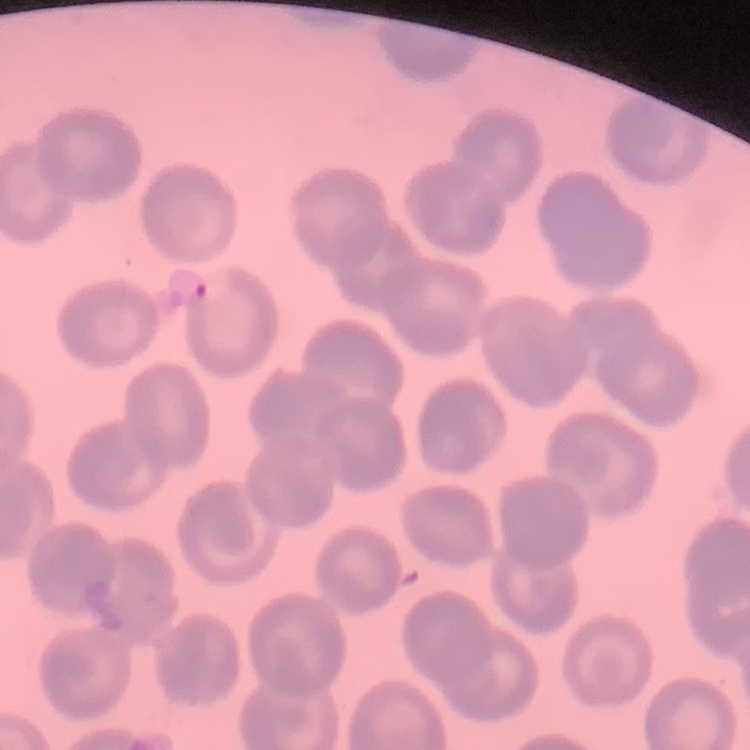
{
  "erythrocyte_morphology": "no rouleaux formation",
  "stain": "Field's or Giemsa",
  "image_type": "square crop of a larger photomicrograph",
  "preparation": "thin blood smear"
}